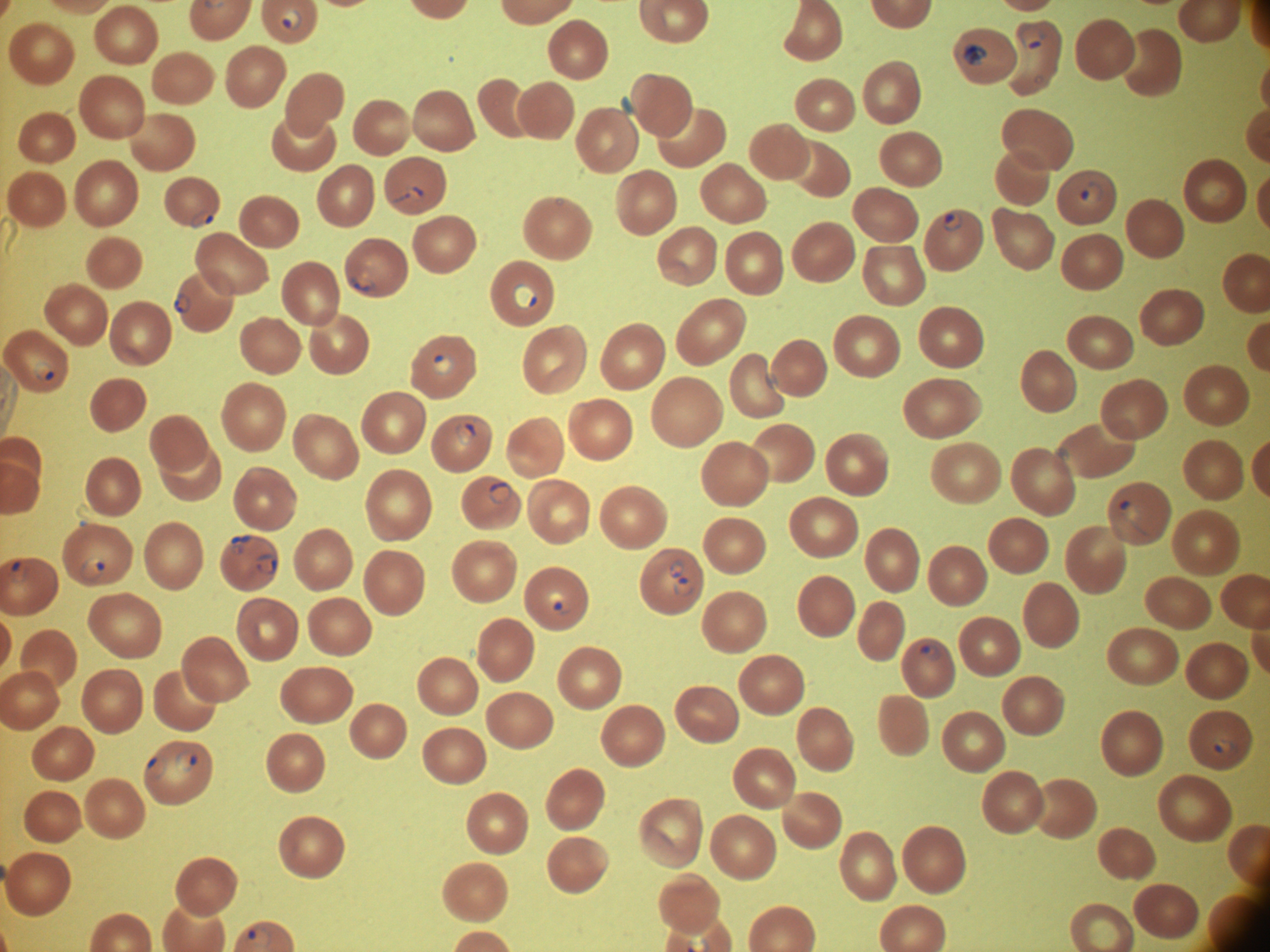
stain: Giemsa
magnification: 100x
image_size: 1270×952 pixels
field_of_view: single
species: Plasmodium falciparum
ring_form_locations: 'approximate bounding boxes as (x1,y1)-(x2,y2) corner pairs in pixels, from the source annotation, which is not necessarily exhaustive: (280,8)-(302,31), (1016,23)-(1045,49), (962,44)-(987,67), (1079,179)-(1103,204), (404,186)-(425,201), (190,211)-(215,229), (942,211)-(963,233), (349,271)-(376,292), (513,283)-(537,310), (173,292)-(192,313), (433,354)-(456,376), (34,360)-(56,381), (456,422)-(477,447), (488,480)-(513,504), (1120,500)-(1140,522), (231,535)-(252,554), (256,553)-(277,574), (79,555)-(106,580), (668,560)-(684,579), (7,561)-(29,583), (674,578)-(694,597), (545,591)-(564,611), (919,644)-(941,662), (1213,738)-(1236,755), (175,748)-(198,773), (145,756)-(167,779), (246,925)-(274,947)'
preparation: thin blood film
microscope: Leica DM2000 with built-in camera